Classify this cell by malaria status.
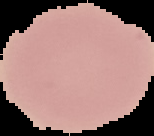

Uninfected.

image size = 154×136 pixels
image type = segmented cell region on a black background
preparation = thin blood film